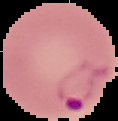

Summary:
  - Result: malaria parasites detected
  - Image size: 118×121 pixels
  - Preparation: thin blood smear
  - Image type: segmented cell region on a black background